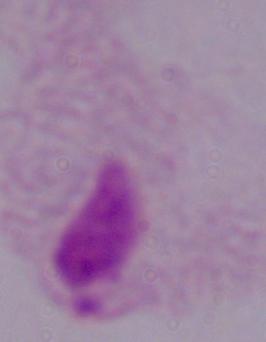
modality = micrograph
identification = trichomonad
magnification = 1000x